Identify the cell.
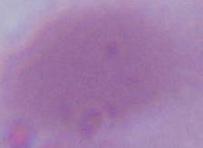
This is an erythrocyte.

1000x magnification. Photomicrograph.